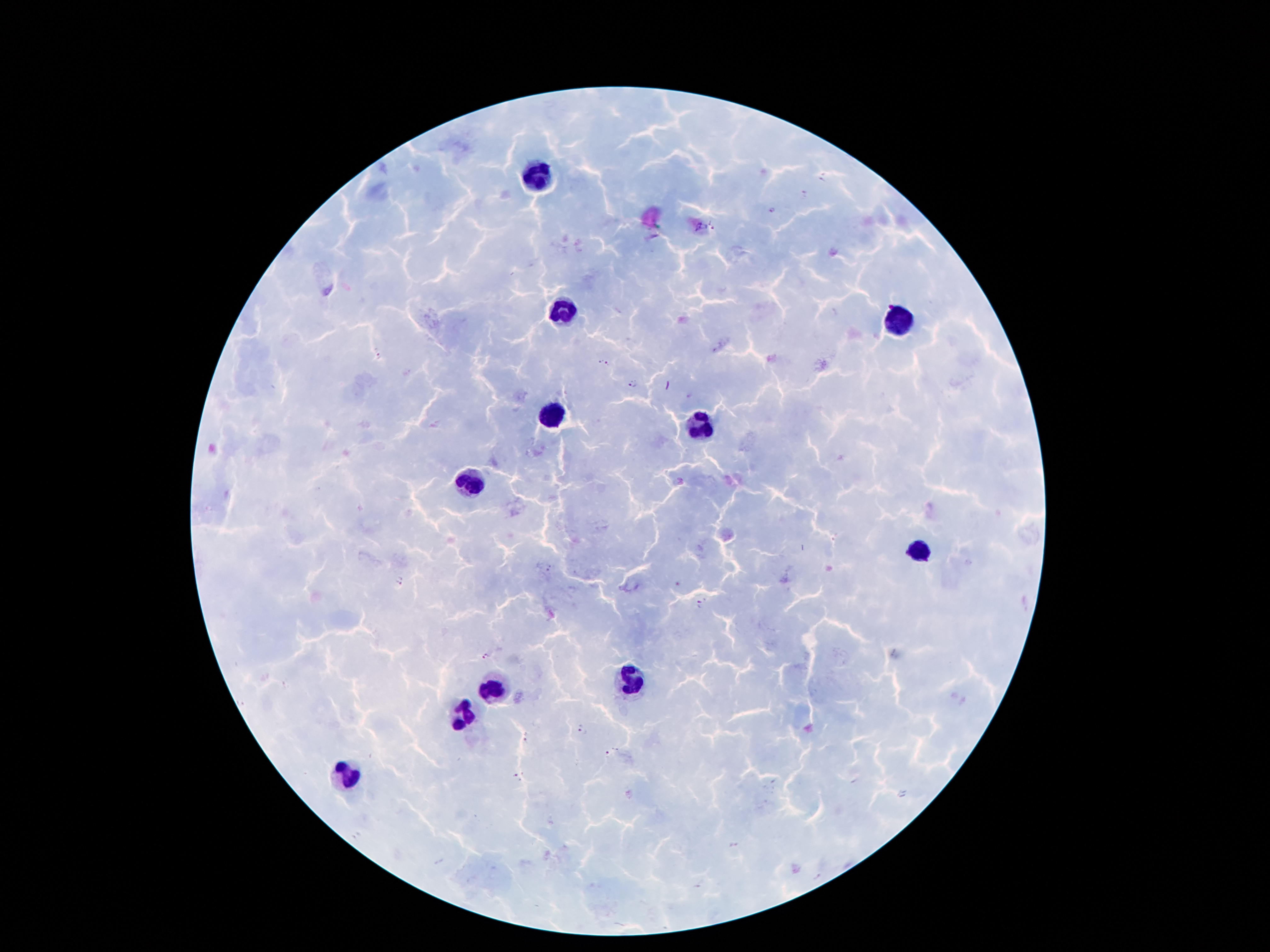

capture: smartphone through the microscope eyepiece
patient_malaria_status: positive for Plasmodium falciparum
magnification: 100x
preparation: thick blood smear
field_of_view: single
stain: Giemsa
image_size: 1270×952 pixels
malaria_parasite_locations: 'approximate centers as [x, y] in pixels: [821, 178], [805, 193], [772, 209], [712, 226], [378, 356], [599, 360], [608, 365], [632, 382], [401, 581], [699, 605], [486, 657], [578, 727], [526, 741], [607, 754], [519, 776]'
leukocyte_locations: 'approximate centers as [x, y] in pixels: [537, 175], [568, 310], [902, 318], [550, 415], [697, 424], [469, 482], [918, 549], [632, 679], [494, 687], [470, 717], [345, 774]'